Describe the morphology of the red blood cells.
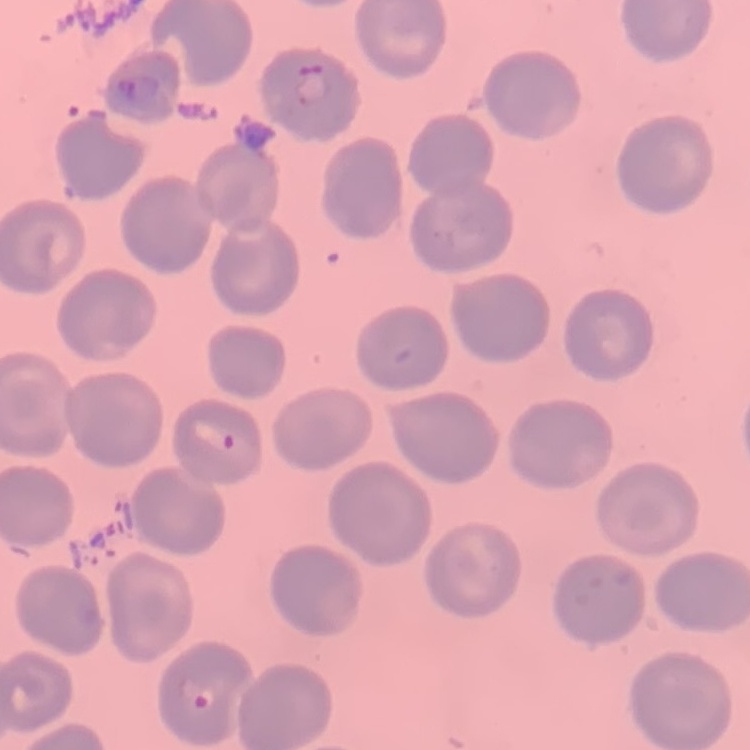

They show no rouleaux formation.

Summary:
  - Image type: one tile cut from a larger photomicrograph
  - Preparation: thin blood smear
  - Stain: Field's or Giemsa